State the preparation type.
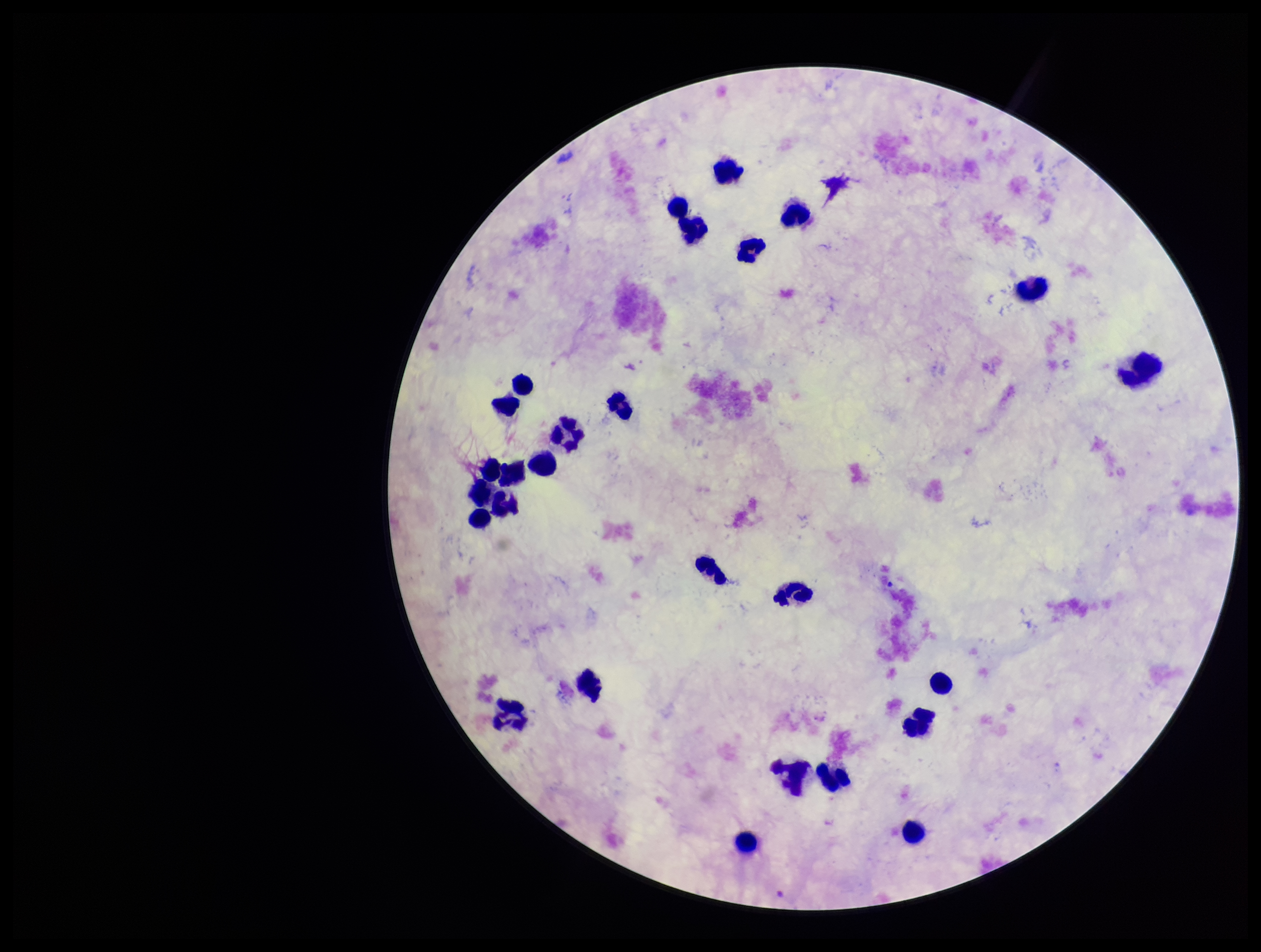

It is a thick blood smear.

Leukocyte count: 27. Smartphone photograph taken through the eyepiece of a microscope. Image is 1261×952 pixels. Single field of view. Giemsa stain. Parasite count: 0. Patient malaria status: negative. Plasmodium parasites: none detected.